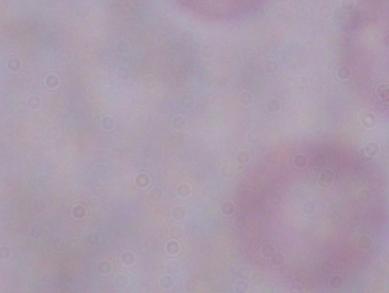

Captured at 1000x magnification. Photomicrograph. A trypanosome is shown.